Assess the morphology of the red blood cells.
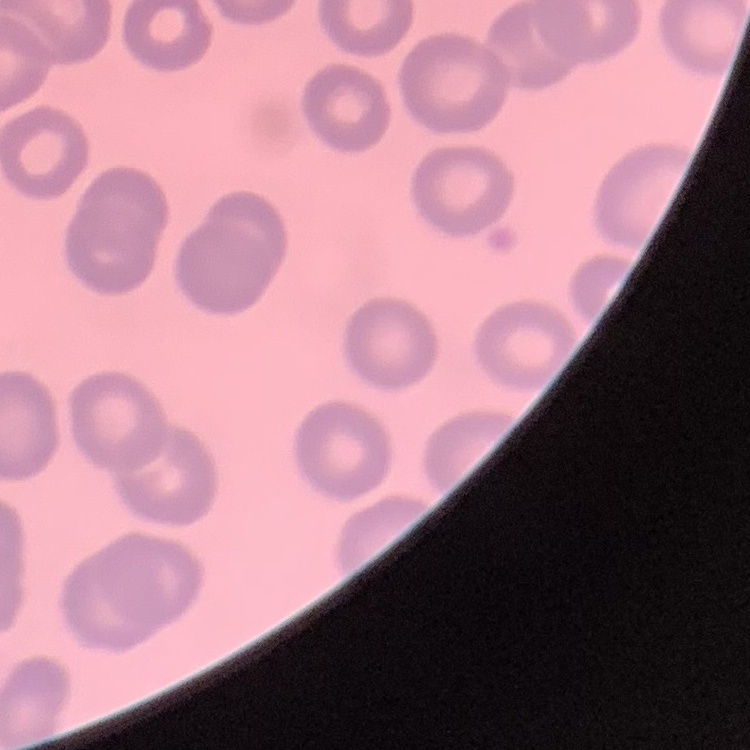
No rouleaux formation.

image type = one tile cut from a larger photomicrograph
preparation = thin blood smear
stain = Field's or Giemsa